Assess this cell for malaria.
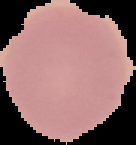
It is uninfected.

Summary:
  - Image type: segmented cell region with the area outside set to black
  - Preparation: thin blood film
  - Image size: 136×145 pixels